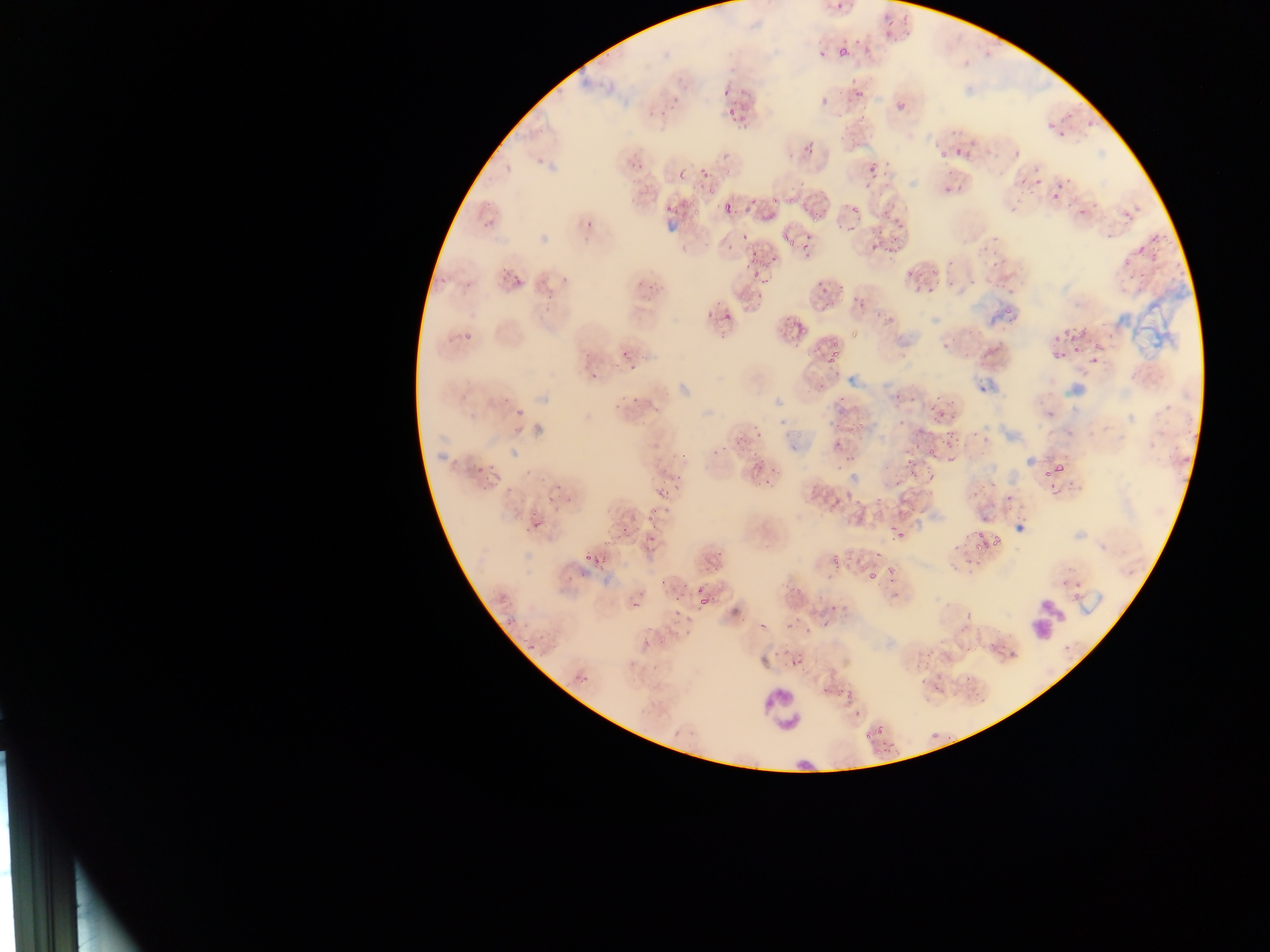
Approximate bounding boxes as (left, top, right, bottom) in pixels. Plasmodium parasite locations (subset; some below the resolvable size): (832, 0, 858, 20), (879, 14, 905, 34), (838, 45, 854, 63), (716, 77, 735, 98), (848, 85, 872, 100), (895, 100, 907, 113), (1055, 105, 1079, 121), (726, 108, 743, 127), (1083, 110, 1101, 131), (1040, 118, 1055, 130), (1053, 128, 1071, 140), (1004, 129, 1033, 161), (949, 133, 978, 159), (800, 143, 817, 155), (937, 149, 947, 159), (866, 151, 893, 187), (1029, 164, 1044, 187), (698, 165, 721, 185), (936, 178, 962, 204), (697, 183, 718, 203), (1045, 183, 1065, 204), (785, 187, 803, 206), (750, 194, 763, 207), (769, 194, 781, 206), (806, 195, 828, 221), (1073, 196, 1085, 213), (715, 199, 739, 221), (664, 200, 680, 215), (690, 203, 704, 219), (846, 205, 870, 237), (880, 210, 908, 234), (477, 218, 498, 238), (584, 218, 595, 230), (982, 225, 1010, 251), (737, 227, 753, 239), (780, 230, 795, 249), (874, 235, 914, 258), (801, 238, 821, 260), (1123, 238, 1152, 270), (742, 243, 776, 280), (938, 257, 960, 291), (983, 259, 1007, 287), (900, 266, 912, 275), (510, 268, 534, 287), (459, 271, 482, 291), (433, 273, 448, 288), (913, 278, 927, 294), (816, 282, 837, 298), (997, 288, 1013, 314), (855, 292, 868, 309), (722, 305, 746, 318), (1065, 317, 1085, 354), (789, 319, 814, 341), (960, 322, 989, 356), (455, 326, 483, 346), (1094, 335, 1115, 363), (1048, 336, 1066, 360), (826, 344, 842, 364), (620, 347, 649, 373), (834, 386, 849, 403), (625, 389, 649, 407), (934, 408, 947, 421), (849, 410, 869, 439), (830, 413, 848, 428), (946, 429, 956, 441), (733, 433, 751, 448), (925, 434, 935, 451), (944, 439, 959, 450), (831, 443, 846, 452), (904, 445, 924, 458), (975, 455, 1015, 497), (472, 458, 490, 478), (746, 458, 771, 476), (1054, 461, 1066, 469), (906, 462, 921, 478), (927, 464, 940, 477), (1045, 468, 1054, 477), (758, 475, 778, 492), (655, 478, 676, 492), (810, 485, 824, 498), (831, 491, 863, 512), (645, 502, 667, 523), (1012, 502, 1036, 523), (523, 509, 551, 530), (887, 511, 907, 539), (619, 521, 637, 533), (971, 532, 982, 549), (645, 536, 661, 551), (988, 536, 1003, 545), (828, 543, 847, 566), (869, 549, 889, 567), (581, 551, 600, 562), (708, 554, 728, 572), (883, 562, 899, 578), (863, 564, 883, 577), (780, 582, 798, 593), (695, 590, 717, 611), (828, 607, 845, 617), (990, 633, 1012, 651), (907, 638, 939, 674), (784, 650, 802, 680), (934, 677, 962, 698), (836, 684, 856, 710), (820, 685, 831, 701), (931, 722, 948, 742), (871, 724, 887, 737), (863, 727, 875, 743), (870, 743, 890, 761). Leukocyte locations: (1026, 593, 1065, 640), (756, 684, 808, 738). Thin blood film. Single field of view. Image is 1270×952 pixels. Mobile-phone photograph taken through the microscope. Sample from Ghana.